Assess this cell for malaria.
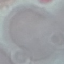
It is uninfected.

Automatically extracted cell patch, resized to 64 × 64 pixels. Giemsa stain. Thin smear of blood. Photographed with a smartphone camera at the microscope eyepiece.